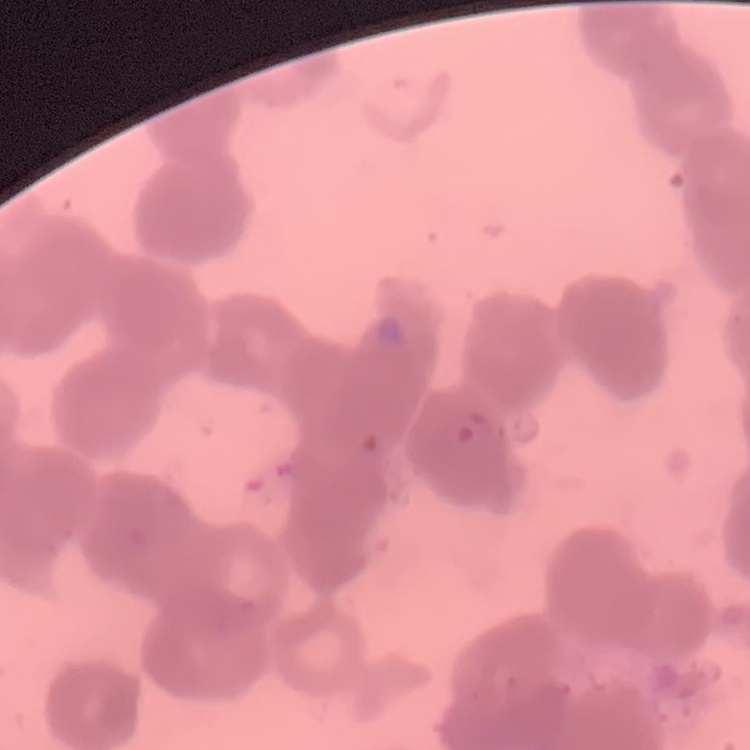

Summary:
  - Red blood cell morphology: rouleaux formation
  - Stain: Field's or Giemsa
  - Preparation: thin peripheral smear
  - Image type: one tile cut from a larger photomicrograph